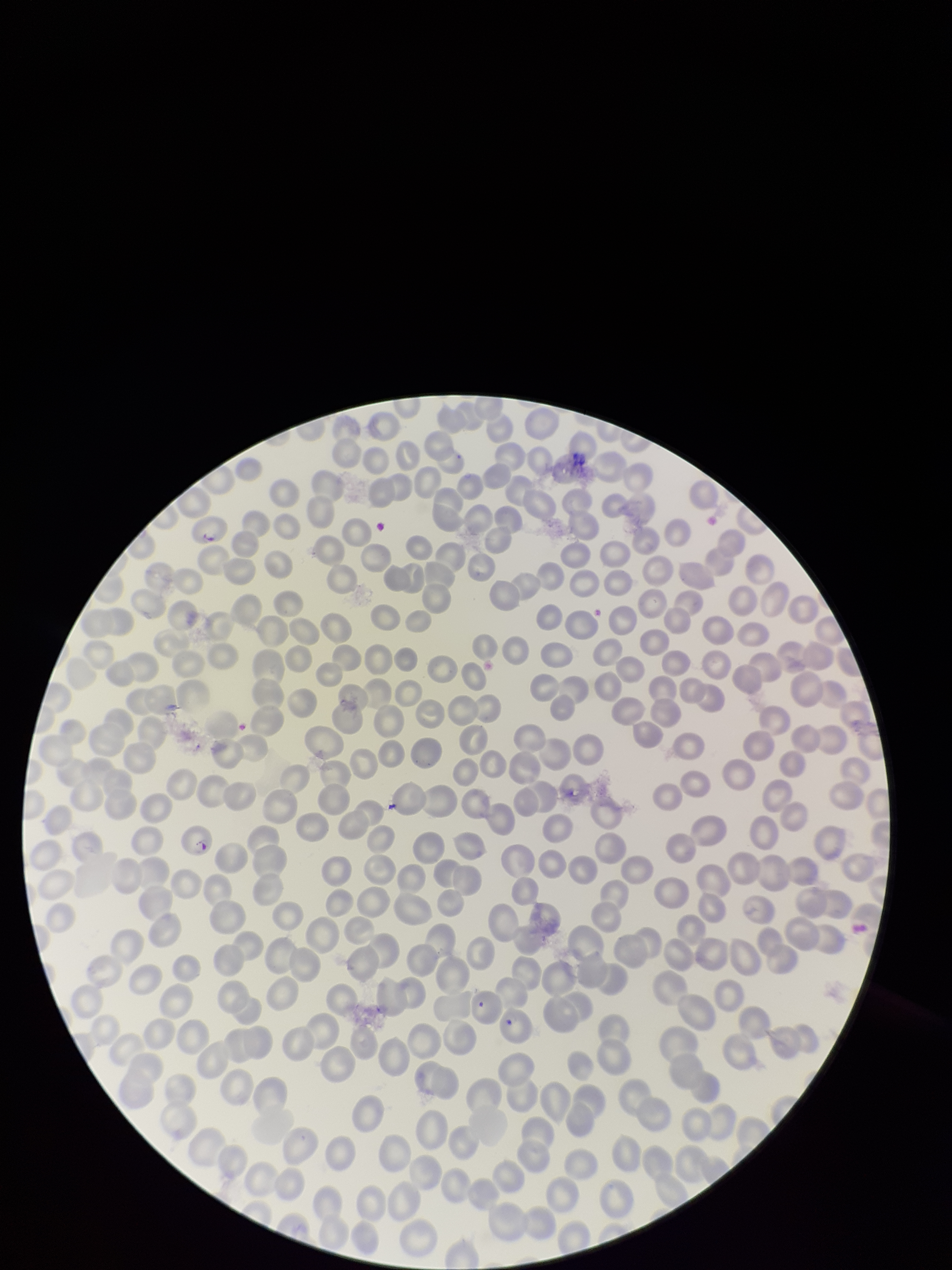
Single field of view. Image is 952×1270 pixels. Patient malaria status: infected. Smartphone photograph taken through the eyepiece of a microscope. Parasitized red blood cell count: 1. Species reported for this patient: Plasmodium falciparum. Red blood cell count: 297. Preparation: thin smear. Giemsa stain. Parasitized red blood cells: seen.